Identify the cell.
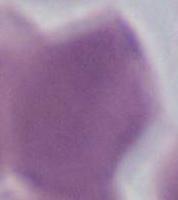
An erythrocyte.

Micrograph. 1000x magnification.